Assess the morphology of the red blood cells.
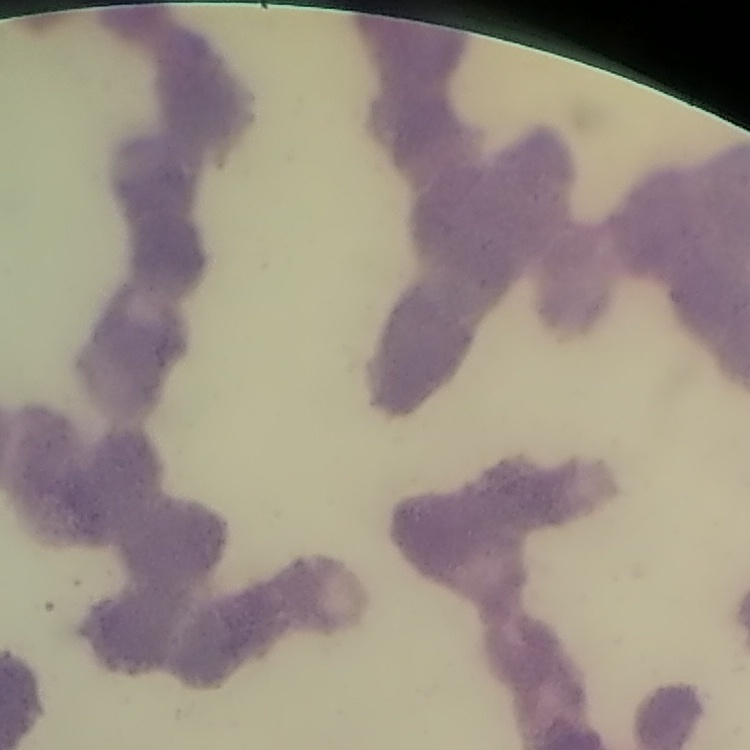
Rouleaux formation.

preparation = thin blood film
image type = square crop of a larger photomicrograph
stain = Field's or Giemsa